Classify this cell by malaria status.
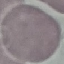
It is uninfected.

Giemsa-stained preparation. Automatically extracted cell patch, resized to 64 × 64 pixels. Thin blood film. Photographed with a smartphone camera at the microscope eyepiece.